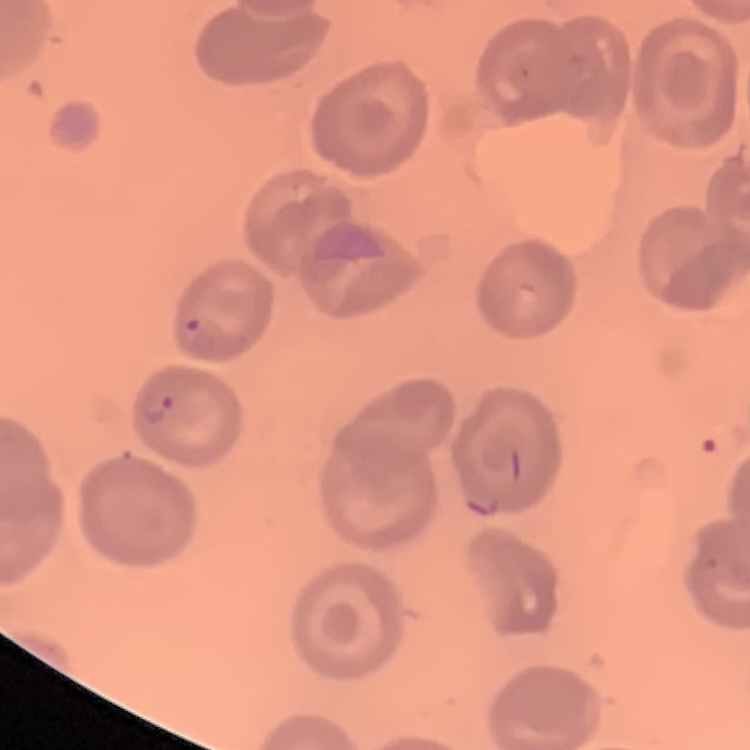

The erythrocytes show no rouleaux formation. One tile cut from a larger photomicrograph. Stained with either Field's or Giemsa. Thin blood smear.